Identify the parasite.
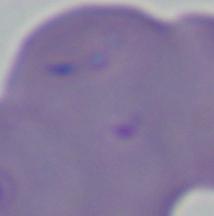

Babesia.

magnification = 1000x
modality = photomicrograph